Assess this cell for malaria.
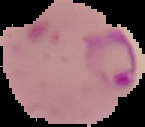
Parasitized.

Summary:
  - Image size: 145×127 pixels
  - Image type: cell region segmented out of the field of view; surrounding area masked to black
  - Preparation: thin blood smear